State the blood parasite species.
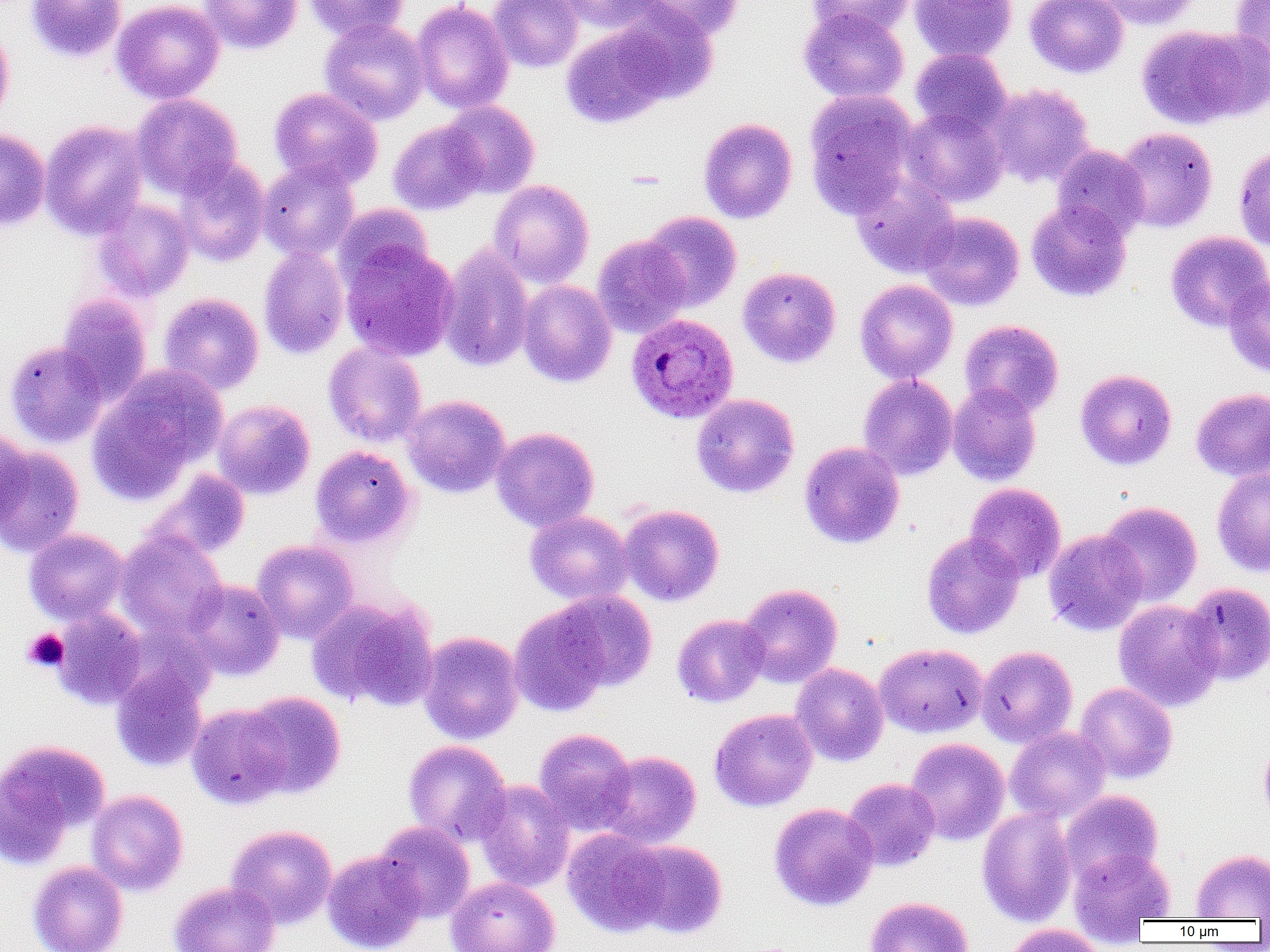
Plasmodium ovale.

uninfected red blood cell locations = approximate bounding boxes as (x1, y1, x2, y2) in pixels: (27, 0, 127, 63), (111, 0, 225, 104), (201, 0, 302, 54), (303, 0, 408, 42), (488, 0, 582, 72), (554, 0, 663, 32), (639, 0, 743, 42), (807, 0, 916, 39), (910, 0, 1017, 63), (1025, 0, 1128, 78), (1090, 0, 1203, 29), (1229, 0, 1270, 77), (410, 1, 514, 114), (610, 6, 719, 104), (799, 8, 909, 103), (319, 19, 429, 125), (562, 24, 673, 128), (1136, 24, 1266, 130), (0, 28, 14, 128), (910, 48, 1012, 137), (987, 83, 1094, 187), (269, 87, 383, 189), (803, 89, 918, 217), (131, 93, 243, 198), (441, 101, 540, 198), (901, 107, 1008, 208), (698, 118, 798, 224), (39, 119, 148, 240), (388, 120, 487, 215), (1114, 127, 1218, 233), (0, 129, 50, 231), (1234, 142, 1270, 252), (1051, 144, 1149, 240), (171, 157, 271, 267), (258, 159, 360, 261), (851, 175, 961, 279), (488, 179, 594, 288), (92, 198, 195, 302), (1026, 199, 1133, 302), (333, 203, 433, 290), (640, 211, 742, 312), (918, 212, 1024, 310), (1165, 231, 1270, 332), (592, 234, 692, 338), (340, 242, 459, 362), (439, 244, 535, 373), (258, 246, 349, 359), (738, 266, 841, 368), (1224, 275, 1270, 378), (855, 279, 959, 384), (517, 280, 618, 387), (55, 293, 152, 402), (159, 293, 264, 395), (959, 319, 1064, 419), (5, 339, 109, 448), (323, 342, 427, 447), (87, 365, 226, 504), (1075, 368, 1177, 470), (858, 374, 958, 481), (947, 384, 1042, 486), (1191, 387, 1270, 481), (691, 393, 800, 498), (402, 395, 511, 498), (212, 399, 315, 500), (490, 427, 599, 531), (0, 429, 33, 526), (799, 441, 905, 549), (0, 446, 85, 558), (310, 446, 417, 549), (1211, 467, 1270, 577), (145, 470, 250, 561), (965, 483, 1066, 583), (1098, 501, 1203, 606), (618, 504, 724, 606), (524, 510, 634, 606), (24, 529, 129, 626), (1043, 529, 1149, 636), (115, 530, 227, 640), (921, 531, 1026, 640), (251, 539, 359, 643), (184, 579, 285, 680), (1182, 582, 1270, 685), (737, 583, 843, 688), (549, 591, 658, 693), (306, 596, 439, 712), (1113, 600, 1224, 711), (508, 603, 612, 718), (51, 610, 147, 710), (672, 614, 769, 707), (418, 631, 524, 744), (874, 643, 988, 738), (976, 645, 1077, 748), (790, 663, 889, 766), (110, 666, 208, 772), (1075, 682, 1177, 784), (239, 691, 347, 799), (187, 703, 292, 809), (709, 708, 818, 812), (533, 727, 636, 834), (1005, 727, 1111, 824), (1259, 736, 1270, 827), (0, 738, 110, 868), (904, 738, 1010, 846), (402, 740, 511, 846), (597, 751, 702, 849), (843, 777, 940, 871), (474, 779, 574, 892), (86, 789, 189, 896), (1060, 790, 1163, 885), (769, 802, 879, 911), (976, 806, 1077, 927), (373, 821, 476, 924), (225, 824, 337, 928), (562, 829, 671, 937), (625, 840, 728, 939), (1068, 848, 1175, 931), (1191, 849, 1270, 920), (322, 850, 426, 952), (28, 860, 129, 952), (446, 876, 560, 952), (169, 880, 280, 952), (865, 896, 974, 952), (1003, 924, 1107, 952)
preparation = thin blood film
field of view = single
image size = 1270×952 pixels
platelet locations = approximate bounding boxes as (x1, y1, x2, y2) in pixels: (23, 628, 69, 672)
magnification = 1000x
modality = optical microscopy
Plasmodium ovale-infected red blood cell locations = approximate bounding boxes as (x1, y1, x2, y2) in pixels: (625, 313, 739, 424)